Comment on the morphology of the erythrocytes.
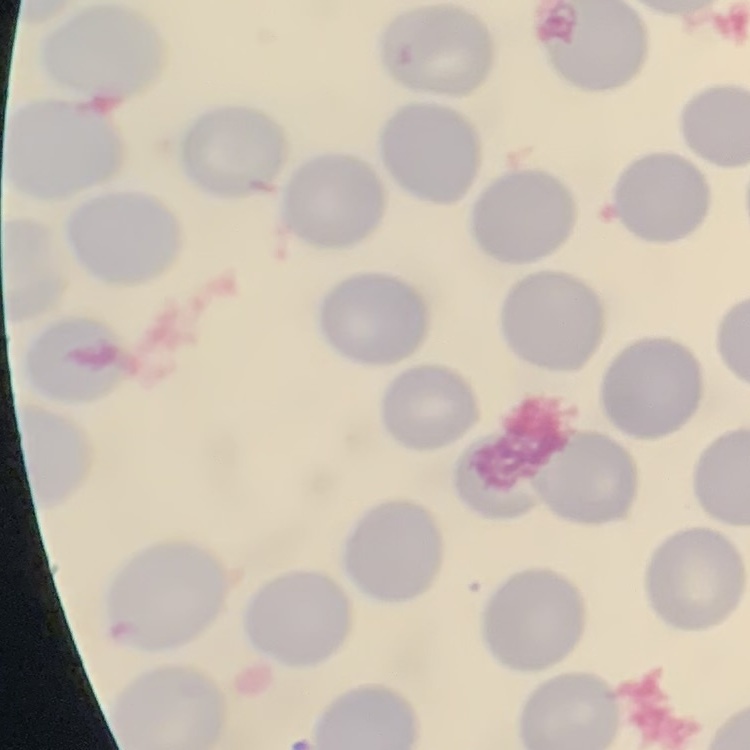

No rouleaux formation.

preparation = thin blood film
image type = square crop of a larger photomicrograph
stain = Field's or Giemsa